Locate every blood parasite and identify its species.
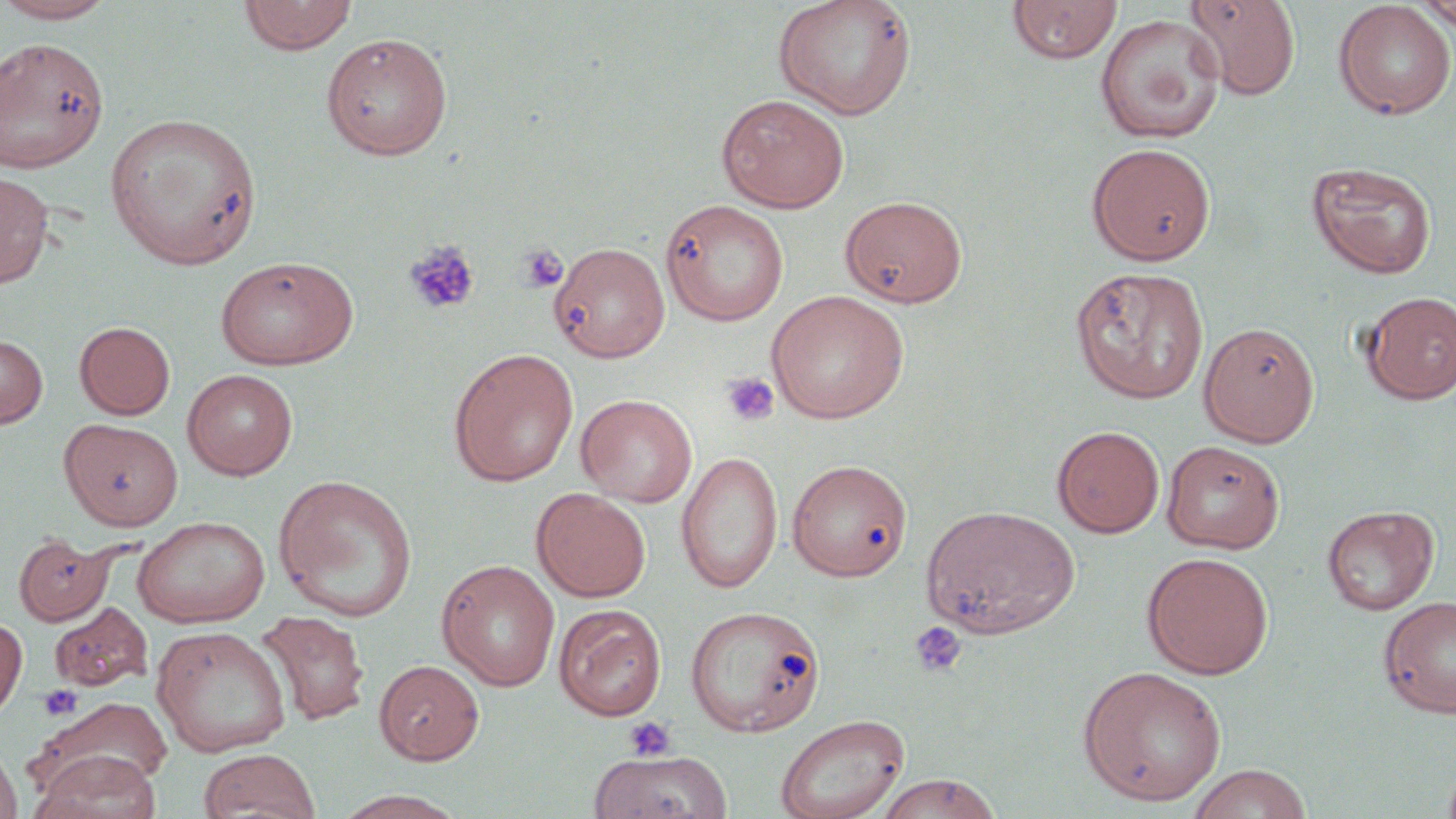
No blood parasites seen.

Approximate bounding boxes as (x1, y1, x2, y2) in pixels. Uninfected red blood cell locations: (0, 0, 119, 23), (238, 0, 359, 55), (773, 0, 917, 120), (1007, 0, 1122, 64), (1183, 0, 1301, 101), (1333, 1, 1456, 120), (1413, 1, 1456, 31), (1095, 14, 1227, 144), (320, 32, 453, 160), (0, 38, 109, 173), (716, 94, 850, 213), (105, 112, 262, 269), (1086, 142, 1217, 265), (1306, 160, 1437, 279), (0, 170, 53, 288), (840, 195, 968, 308), (660, 199, 789, 327), (549, 242, 670, 362), (215, 255, 359, 370), (1070, 267, 1210, 404), (766, 291, 909, 424), (1359, 291, 1456, 404), (74, 321, 176, 420), (1198, 321, 1320, 447), (0, 334, 48, 428), (448, 348, 579, 487), (182, 368, 299, 480), (576, 394, 697, 507), (59, 418, 183, 531), (1052, 425, 1165, 537), (1161, 440, 1285, 554), (677, 450, 783, 593), (786, 459, 912, 580), (274, 474, 418, 621), (531, 487, 651, 602), (545, 488, 659, 720), (921, 504, 1080, 639), (1321, 504, 1439, 615), (132, 516, 269, 627), (13, 533, 114, 625), (1141, 552, 1274, 679), (437, 560, 560, 691), (1377, 594, 1456, 719), (48, 602, 152, 692), (553, 604, 667, 721), (685, 605, 826, 737), (256, 611, 370, 726), (0, 614, 27, 724), (151, 626, 292, 757), (375, 659, 484, 765), (1077, 665, 1227, 806), (26, 697, 174, 804), (774, 713, 909, 819), (0, 739, 23, 819), (198, 749, 321, 819), (30, 751, 161, 819), (587, 751, 733, 819), (1441, 755, 1456, 819), (1185, 763, 1314, 819), (873, 773, 1003, 819), (330, 790, 471, 819). Platelet locations: (404, 240, 481, 315), (518, 243, 569, 294), (720, 371, 780, 428), (909, 621, 968, 677), (39, 684, 82, 721), (622, 716, 675, 761). Slide-level diagnosis: negative for blood parasites. Captured at 1000x magnification. One field of a larger specimen. Optical microscopy. Image is 1456×819 pixels. Thin blood smear. May-Grünwald-Giemsa stain.